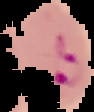
Malaria status: parasitized. The area outside the segmented cell region is set to black. Image is 94×112 pixels. From a thin blood smear.